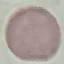

result = no malaria parasites detected
stain = Giemsa
preparation = thin blood smear
capture = smartphone through the microscope eyepiece
image type = cell patch, automatically extracted from a larger field of view and resized to 64 × 64 pixels